Name the parasite shown.
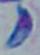

This is Toxoplasma gondii.

Summary:
  - Magnification: 1000x
  - Modality: photomicrograph